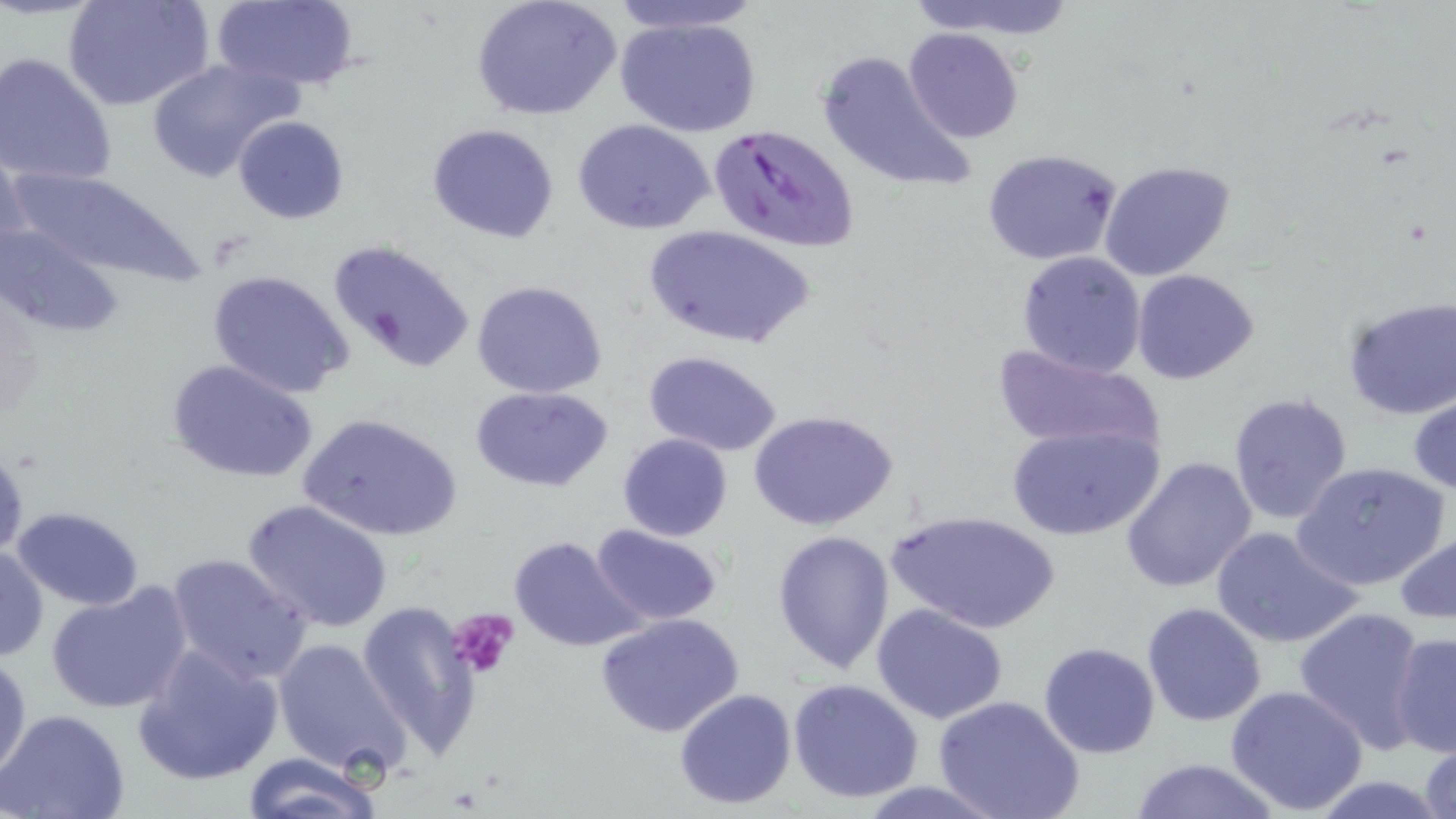

Approximate bounding boxes as [x1, y1, x2, y2] in pixels. Uninfected red blood cell locations: [63, 0, 213, 111], [208, 0, 360, 90], [470, 0, 622, 121], [604, 0, 769, 35], [907, 0, 1082, 44], [615, 16, 765, 138], [902, 28, 1022, 144], [815, 48, 978, 197], [0, 52, 119, 187], [146, 57, 302, 183], [232, 115, 349, 224], [573, 118, 716, 236], [426, 124, 560, 244], [982, 148, 1121, 267], [1099, 160, 1239, 283], [5, 169, 203, 281], [1, 221, 126, 342], [644, 225, 814, 350], [324, 238, 475, 375], [1014, 250, 1147, 377], [206, 268, 356, 398], [1130, 268, 1259, 384], [469, 280, 609, 400], [1340, 296, 1456, 419], [996, 346, 1159, 455], [643, 351, 784, 457], [166, 359, 318, 485], [469, 386, 613, 492], [1227, 390, 1355, 527], [1409, 393, 1455, 494], [750, 410, 899, 532], [297, 412, 463, 541], [1007, 423, 1162, 542], [617, 433, 732, 541], [0, 449, 28, 559], [1120, 457, 1257, 593], [1290, 460, 1451, 592], [242, 498, 394, 632], [10, 505, 145, 611], [886, 510, 1060, 634], [590, 524, 724, 627], [1209, 524, 1362, 649], [1394, 526, 1456, 626], [771, 528, 893, 674], [507, 534, 646, 654], [0, 546, 47, 663], [165, 551, 313, 685], [46, 584, 191, 714], [357, 600, 482, 758], [1141, 601, 1267, 727], [871, 602, 1010, 725], [1294, 606, 1430, 751], [594, 612, 746, 739], [1389, 631, 1455, 757], [272, 636, 412, 778], [1039, 641, 1161, 758], [133, 643, 284, 787], [1, 651, 30, 785], [787, 677, 924, 804], [1225, 685, 1369, 815], [674, 687, 798, 811], [933, 695, 1084, 819], [0, 708, 131, 819], [1416, 738, 1456, 819], [240, 752, 383, 819], [1126, 756, 1284, 819], [852, 780, 1009, 818]. Platelet locations: [448, 609, 519, 678]. Plasmodium falciparum-infected red blood cell locations: [708, 123, 860, 255]. Slide-level diagnosis: Plasmodium falciparum. 1000x magnification. One field of a larger specimen. Image is 1456×819 pixels. May-Grünwald-Giemsa-stained preparation. Optical microscopy. Thin blood film.